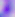

Toxoplasma gondii is shown. Captured at 400x magnification. Micrograph.